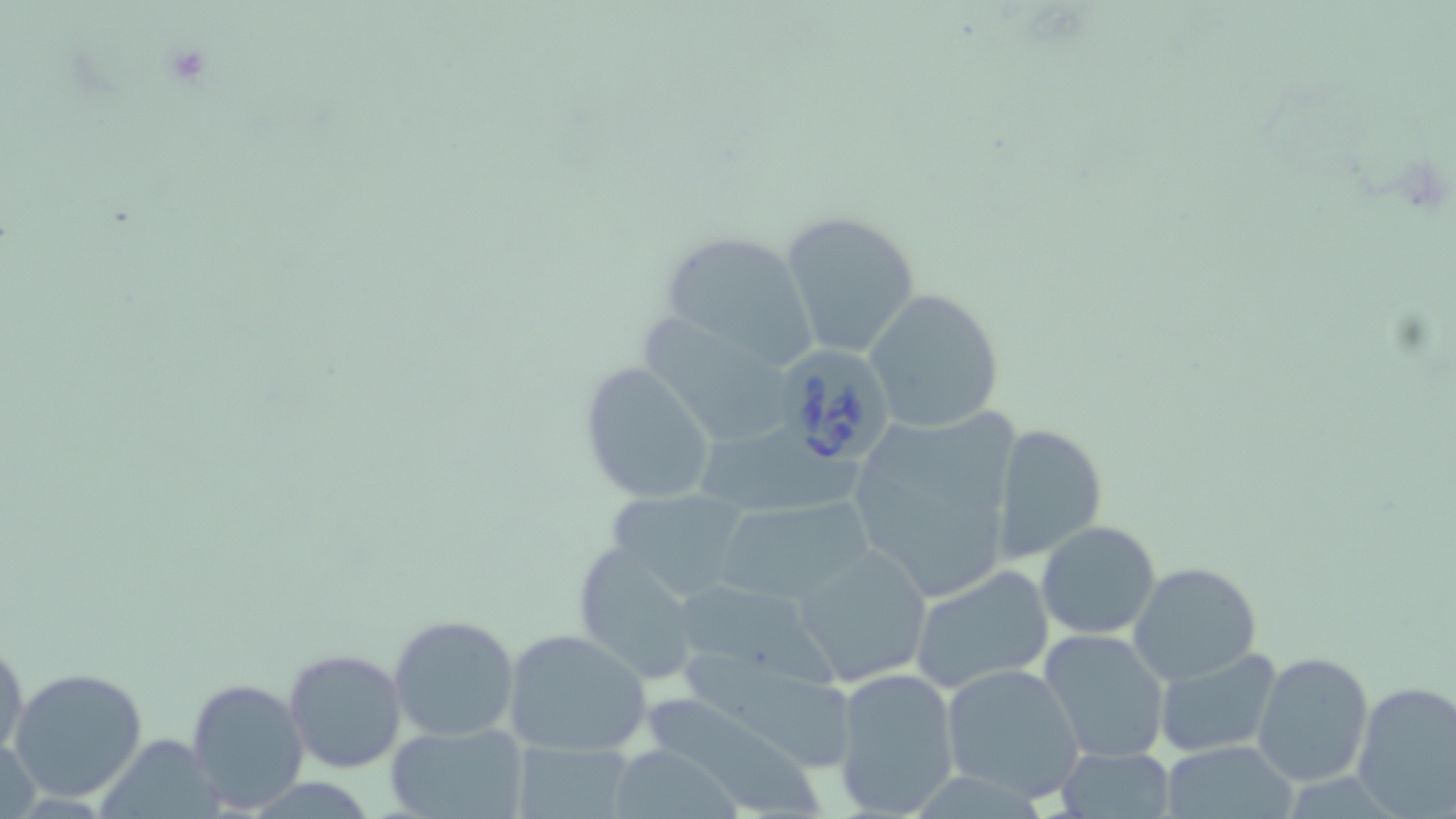

slide-level diagnosis = Babesia divergens
field of view = single
magnification = 1000x
image size = 1456×819 pixels
stain = May-Grünwald-Giemsa
Babesia divergens-infected red blood cell locations = approximate bounding boxes as (x1, y1, x2, y2) in pixels: (764, 347, 895, 472)
uninfected red blood cell locations = approximate bounding boxes as (x1, y1, x2, y2) in pixels: (779, 210, 921, 363), (654, 229, 819, 375), (862, 288, 1004, 433), (645, 316, 800, 446), (578, 362, 717, 505), (847, 412, 1023, 602), (988, 422, 1107, 565), (708, 426, 866, 521), (602, 487, 759, 606), (714, 500, 870, 605), (1035, 521, 1162, 639), (793, 544, 933, 686), (577, 549, 689, 668), (1127, 562, 1262, 684), (910, 565, 1055, 693), (680, 583, 849, 697), (389, 612, 521, 743), (502, 628, 651, 755), (1037, 628, 1171, 764), (0, 632, 26, 760), (1151, 646, 1285, 759), (284, 648, 409, 775), (679, 649, 853, 767), (1251, 650, 1376, 788), (939, 663, 1088, 803), (8, 666, 150, 802), (831, 666, 962, 818), (185, 676, 311, 814), (1351, 682, 1456, 815), (653, 694, 826, 819), (100, 724, 224, 819), (385, 724, 529, 819), (0, 739, 43, 819), (508, 740, 637, 818), (1158, 740, 1297, 818), (621, 743, 741, 816), (1055, 744, 1177, 817)
modality = optical microscopy
preparation = thin blood smear